Assess this cell for malaria.
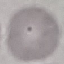

It is uninfected.

Summary:
  - Stain: Giemsa
  - Image type: cell patch, automatically extracted from a larger field of view and resized to 64 × 64 pixels
  - Capture: smartphone through the microscope eyepiece
  - Preparation: thin blood smear